Assess the background quality.
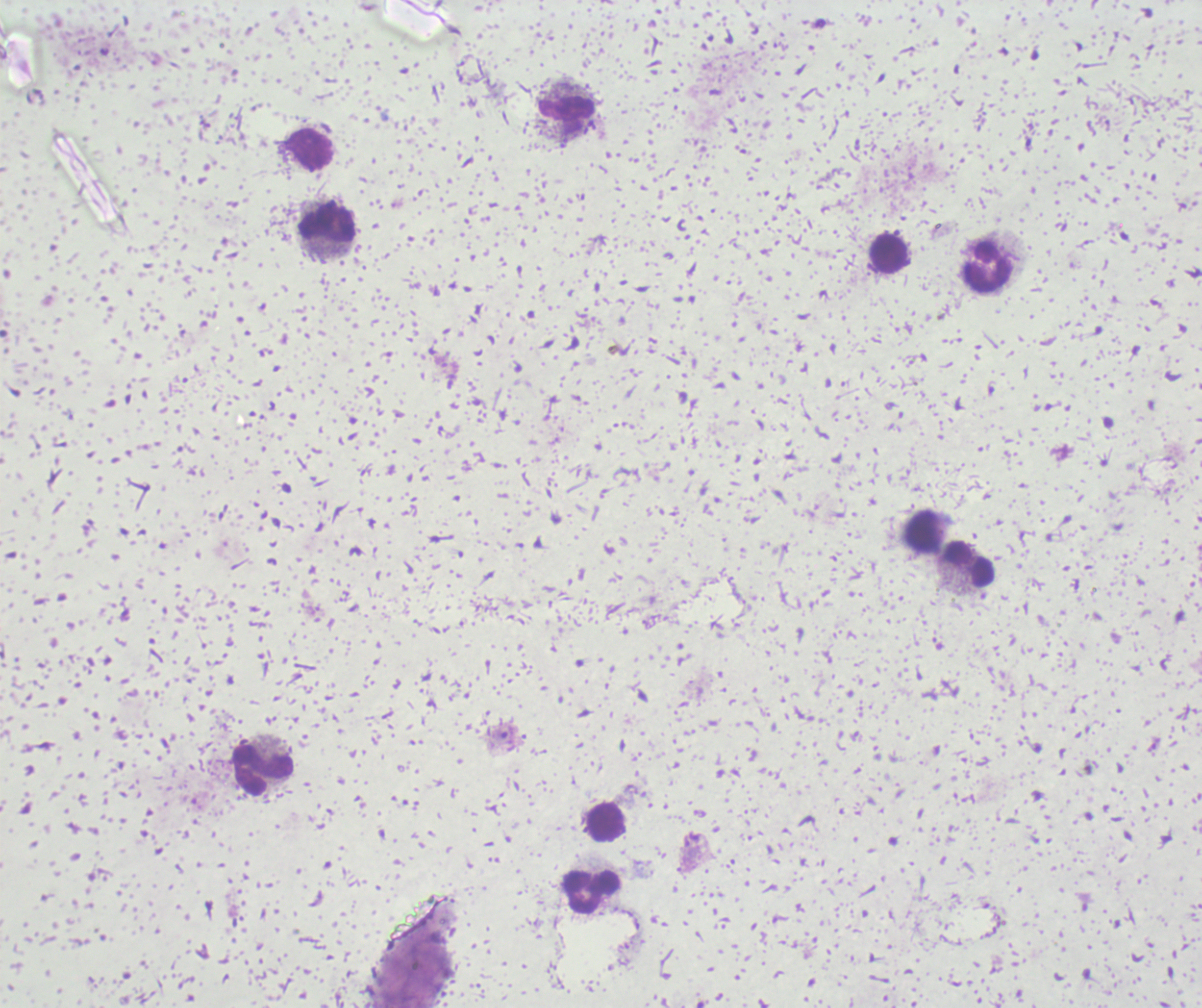

Poor.

coordinate format = approximate centers as {x, y} in pixels
leukocyte locations = {566, 114}, {309, 149}, {327, 223}, {890, 254}, {988, 269}, {923, 530}, {969, 562}, {262, 770}, {605, 822}, {591, 891}
result = negative for Plasmodium parasites
preparation = thick blood film
image size = 1202×1008 pixels
stain = Romanowsky
magnification = 100x
context = previously used in an actual diagnosis
field of view = single